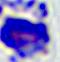
magnification = 400x
identification = leukocyte
modality = photomicrograph